Locate every blood parasite and identify its species.
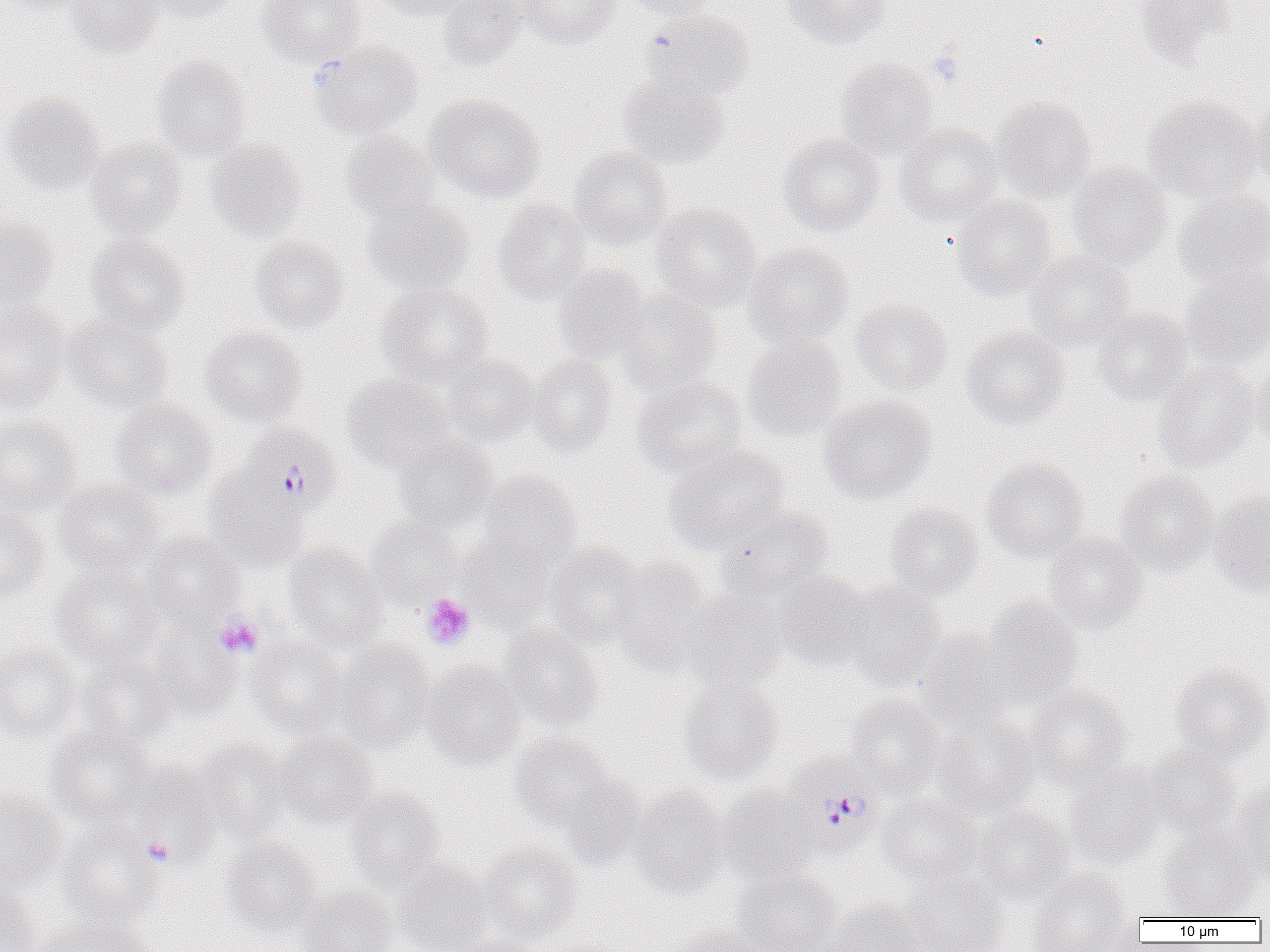
Approximate bounding boxes as (x1,y1)-(x2,y2) corner pairs in pixels.
Plasmodium falciparum-infected red blood cells: (240,423)-(342,517), (786,756)-(881,851).
No Plasmodium ovale, Plasmodium malariae, Plasmodium vivax, Babesia divergens, or Trypanosoma brucei observed.

Summary:
  - Uninfected red blood cell locations: (0,0)-(94,15), (67,0)-(164,58), (146,0)-(246,22), (257,0)-(364,67), (372,0)-(473,20), (437,0)-(529,72), (519,0)-(619,49), (623,0)-(717,21), (781,0)-(893,49), (1132,0)-(1236,69), (642,9)-(755,102), (309,40)-(424,139), (153,56)-(251,161), (836,58)-(938,159), (619,74)-(729,169), (1,93)-(106,196), (423,94)-(545,203), (990,96)-(1096,205), (1142,96)-(1265,204), (1247,100)-(1270,201), (894,122)-(1003,226), (340,132)-(444,225), (778,133)-(884,237), (86,138)-(188,239), (205,139)-(307,242), (569,146)-(672,250), (1068,161)-(1174,270), (1172,191)-(1270,287), (952,195)-(1057,302), (363,199)-(474,297), (493,199)-(592,304), (650,202)-(762,311), (0,219)-(58,309), (84,234)-(188,335), (250,236)-(349,334), (742,243)-(854,348), (1024,250)-(1137,351), (553,264)-(649,365), (1181,266)-(1270,368), (375,285)-(493,386), (614,289)-(721,395), (850,298)-(953,395), (0,301)-(69,413), (1093,309)-(1194,406), (64,315)-(173,412), (201,326)-(307,428), (962,326)-(1069,430), (742,335)-(846,441), (444,354)-(541,446), (526,354)-(618,458), (1250,357)-(1270,451), (1153,360)-(1259,473), (343,374)-(454,473), (631,377)-(748,478), (818,394)-(936,504), (109,401)-(216,500), (0,417)-(82,518), (394,436)-(497,532), (664,444)-(790,552), (982,458)-(1089,563), (203,469)-(308,571), (478,471)-(584,568), (1115,471)-(1220,574), (53,478)-(163,576), (1208,490)-(1270,597), (885,504)-(984,601), (714,507)-(834,601), (0,508)-(51,605), (365,515)-(462,607), (142,532)-(244,627), (1043,533)-(1148,634), (457,535)-(553,631), (543,542)-(645,648), (285,544)-(388,653), (611,558)-(715,674), (51,563)-(163,668), (772,571)-(871,670), (843,583)-(946,690), (681,593)-(787,694), (982,596)-(1083,704), (499,627)-(604,730), (150,628)-(240,718), (916,629)-(1018,728), (247,635)-(347,737), (334,642)-(435,753), (0,644)-(83,743), (76,655)-(176,747), (421,661)-(526,769), (1170,665)-(1270,762), (677,679)-(784,785), (1023,685)-(1133,791), (847,696)-(943,795), (934,712)-(1038,819), (45,728)-(155,828), (275,731)-(378,827), (511,735)-(618,834), (196,740)-(293,842), (1142,744)-(1242,837), (126,763)-(225,856), (1066,766)-(1166,868), (554,771)-(646,869), (716,786)-(820,884), (1226,787)-(1270,883), (628,788)-(730,898), (346,789)-(444,892), (0,790)-(68,893), (878,794)-(983,887), (972,808)-(1075,904), (55,820)-(165,929), (1157,826)-(1263,920), (220,838)-(323,936), (478,842)-(584,941), (392,860)-(492,952), (1027,869)-(1140,952), (733,871)-(841,952), (903,875)-(1010,952), (0,884)-(42,952), (298,885)-(398,952), (825,899)-(920,952), (34,914)-(161,952), (667,925)-(766,952), (456,934)-(543,952)
  - Platelet locations: (928,47)-(965,87), (420,593)-(476,650), (213,614)-(263,659), (142,837)-(175,867)
  - Slide-level diagnosis: Plasmodium falciparum
  - Preparation: thin blood smear
  - Magnification: 1000x
  - Image size: 1270×952 pixels
  - Field of view: one of a larger specimen
  - Modality: light microscopy